Locate and identify every blood parasite.
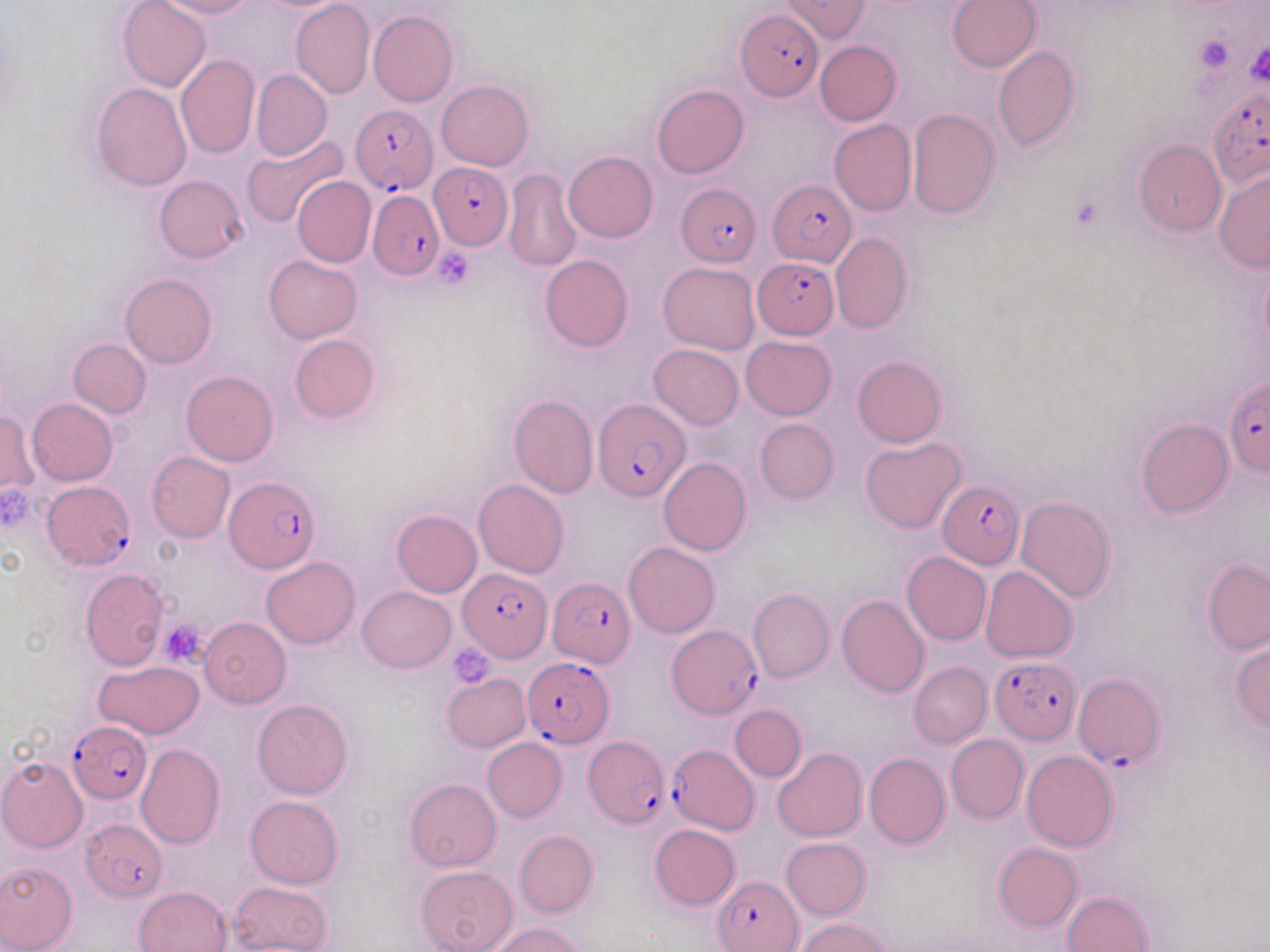
Approximate bounding boxes as (x1,y1)-(x2,y2) corner pairs in pixels.
Plasmodium falciparum-infected red blood cells: (735,7)-(822,100), (1208,88)-(1270,189), (349,104)-(437,195), (428,165)-(514,250), (767,180)-(852,266), (677,183)-(760,266), (368,190)-(442,280), (752,256)-(839,339), (1223,379)-(1270,475), (593,399)-(691,501), (223,476)-(317,574), (42,480)-(135,569), (938,481)-(1025,567), (459,569)-(549,661), (548,576)-(634,666), (666,625)-(762,719), (991,656)-(1080,745), (521,658)-(612,747), (1072,672)-(1163,770), (68,721)-(152,803), (584,734)-(669,827), (668,743)-(760,834), (81,818)-(168,901), (717,875)-(804,951).
No Plasmodium ovale, Plasmodium malariae, Plasmodium vivax, Babesia divergens, or Trypanosoma brucei observed.

{
  "slide_level_diagnosis": "Plasmodium falciparum",
  "uninfected_red_blood_cell_locations": "approximate bounding boxes as (x1,y1)-(x2,y2) corner pairs in pixels: (117,0)-(209,92), (159,0)-(254,20), (290,0)-(375,99), (780,0)-(870,41), (947,0)-(1041,72), (368,11)-(458,107), (816,41)-(901,125), (993,47)-(1079,152), (175,54)-(260,159), (252,71)-(332,161), (436,79)-(534,170), (91,82)-(192,191), (652,83)-(748,179), (906,108)-(1000,220), (829,120)-(917,216), (241,133)-(347,230), (1134,139)-(1226,236), (563,149)-(658,242), (503,168)-(582,272), (1213,169)-(1270,273), (156,175)-(247,262), (292,176)-(376,267), (830,232)-(911,333), (263,254)-(363,343), (540,255)-(633,352), (658,261)-(760,356), (120,273)-(217,369), (290,333)-(380,422), (741,336)-(836,419), (68,338)-(152,419), (648,343)-(743,429), (852,355)-(947,447), (181,370)-(279,466), (508,392)-(598,497), (26,398)-(118,485), (0,412)-(40,494), (755,418)-(839,503), (1136,418)-(1234,517), (861,437)-(967,534), (146,451)-(235,542), (658,456)-(751,555), (473,479)-(569,579), (1016,495)-(1117,602), (391,509)-(482,597), (624,543)-(719,638), (901,552)-(992,644), (261,555)-(360,648), (1203,558)-(1270,655), (980,565)-(1077,662), (79,568)-(169,671), (358,586)-(456,672), (748,588)-(834,682), (837,595)-(930,698), (199,617)-(292,709), (1230,639)-(1270,732), (94,661)-(204,739), (909,661)-(991,747), (442,673)-(530,751), (253,698)-(352,799), (730,704)-(805,781), (945,734)-(1028,823), (482,738)-(567,821), (135,744)-(225,850), (772,747)-(867,841), (1022,750)-(1118,850), (864,752)-(951,848), (0,756)-(89,852), (405,778)-(501,870), (245,795)-(343,888), (649,823)-(741,911), (515,830)-(598,917), (781,837)-(871,919), (993,841)-(1083,930), (0,860)-(78,952), (416,866)-(519,952), (231,882)-(331,951), (134,886)-(232,952), (1061,891)-(1154,952), (797,918)-(892,952), (491,923)-(584,952)",
  "modality": "light microscopy",
  "stain": "May-Grünwald-Giemsa",
  "magnification": "1000x",
  "platelet_locations": "approximate bounding boxes as (x1,y1)-(x2,y2) corner pairs in pixels: (1196,34)-(1235,72), (1246,42)-(1268,87), (434,249)-(475,290), (2,481)-(39,529), (158,619)-(210,668), (450,642)-(497,686)",
  "field_of_view": "single",
  "preparation": "thin blood smear",
  "image_size": "1270×952 pixels"
}